Classify this cell by malaria status.
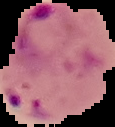
Parasitized.

Image is 115×127 pixels. From a thin blood film. Segmented cell region on a black background.